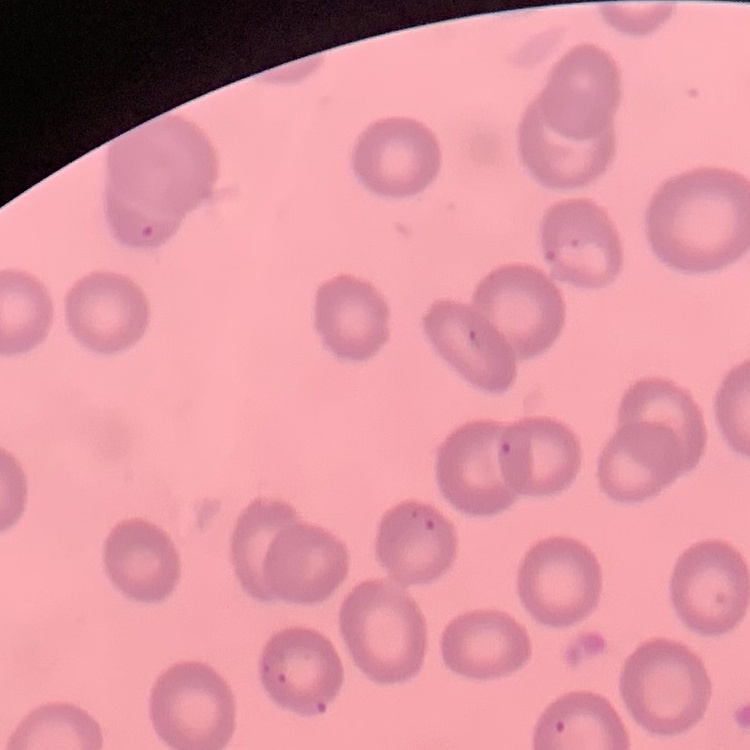
Summary:
  - Red blood cell morphology: no rouleaux formation
  - Preparation: thin blood film
  - Stain: Field's or Giemsa
  - Image type: square crop of a larger photomicrograph